Locate every blood parasite and identify its species.
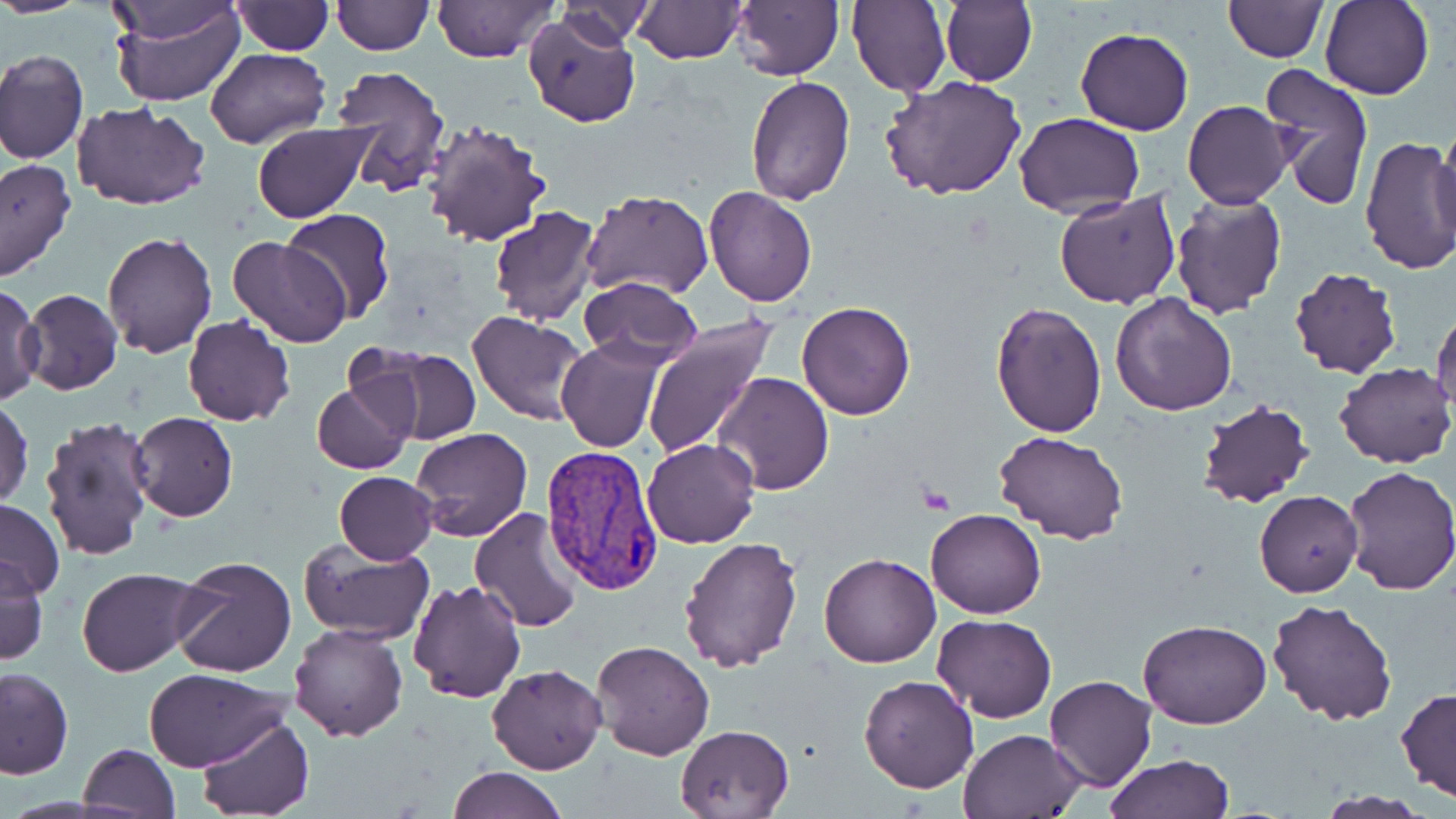

Approximate bounding boxes as named x1/y1/x2/y2 corners in pixels.
Plasmodium vivax-infected red blood cells: (x1=538, y1=447, x2=665, y2=597).
No Plasmodium falciparum, Plasmodium ovale, Plasmodium malariae, Babesia divergens, or Trypanosoma brucei observed.

slide-level diagnosis = Plasmodium vivax
preparation = thin blood smear
modality = light microscopy
field of view = single
stain = May-Grünwald-Giemsa
uninfected red blood cell locations = approximate bounding boxes as named x1/y1/x2/y2 corners in pixels: (x1=0, y1=0, x2=88, y2=18), (x1=108, y1=0, x2=246, y2=109), (x1=330, y1=0, x2=432, y2=55), (x1=732, y1=0, x2=844, y2=81), (x1=849, y1=0, x2=951, y2=98), (x1=940, y1=0, x2=1037, y2=87), (x1=1224, y1=0, x2=1327, y2=61), (x1=1321, y1=0, x2=1435, y2=101), (x1=103, y1=1, x2=247, y2=47), (x1=231, y1=1, x2=333, y2=54), (x1=429, y1=1, x2=558, y2=62), (x1=551, y1=1, x2=655, y2=51), (x1=635, y1=1, x2=744, y2=63), (x1=524, y1=11, x2=640, y2=128), (x1=1075, y1=27, x2=1193, y2=135), (x1=205, y1=48, x2=328, y2=148), (x1=0, y1=50, x2=87, y2=166), (x1=1260, y1=62, x2=1376, y2=210), (x1=329, y1=63, x2=452, y2=197), (x1=880, y1=74, x2=1027, y2=200), (x1=744, y1=75, x2=855, y2=207), (x1=1183, y1=100, x2=1291, y2=206), (x1=72, y1=102, x2=210, y2=211), (x1=1013, y1=111, x2=1145, y2=217), (x1=420, y1=117, x2=551, y2=248), (x1=252, y1=121, x2=373, y2=223), (x1=1434, y1=128, x2=1456, y2=239), (x1=1359, y1=137, x2=1456, y2=275), (x1=0, y1=158, x2=75, y2=283), (x1=702, y1=186, x2=818, y2=307), (x1=582, y1=190, x2=714, y2=300), (x1=1054, y1=192, x2=1182, y2=309), (x1=1170, y1=192, x2=1288, y2=319), (x1=490, y1=207, x2=600, y2=326), (x1=281, y1=210, x2=396, y2=324), (x1=101, y1=231, x2=216, y2=357), (x1=227, y1=237, x2=351, y2=348), (x1=1288, y1=268, x2=1402, y2=381), (x1=578, y1=276, x2=701, y2=368), (x1=1, y1=284, x2=43, y2=404), (x1=20, y1=288, x2=122, y2=395), (x1=1110, y1=292, x2=1238, y2=415), (x1=992, y1=300, x2=1107, y2=436), (x1=796, y1=302, x2=917, y2=421), (x1=1432, y1=306, x2=1456, y2=416), (x1=468, y1=310, x2=591, y2=425), (x1=182, y1=315, x2=296, y2=427), (x1=641, y1=316, x2=776, y2=460), (x1=556, y1=338, x2=667, y2=453), (x1=360, y1=345, x2=481, y2=445), (x1=1334, y1=363, x2=1455, y2=468), (x1=713, y1=372, x2=834, y2=494), (x1=313, y1=382, x2=413, y2=474), (x1=1, y1=396, x2=34, y2=509), (x1=1193, y1=397, x2=1316, y2=510), (x1=128, y1=413, x2=238, y2=522), (x1=39, y1=418, x2=158, y2=564), (x1=410, y1=428, x2=532, y2=543), (x1=994, y1=430, x2=1128, y2=544), (x1=642, y1=438, x2=759, y2=549), (x1=1339, y1=464, x2=1456, y2=595), (x1=334, y1=470, x2=437, y2=564), (x1=1255, y1=490, x2=1362, y2=598), (x1=0, y1=499, x2=65, y2=599), (x1=468, y1=506, x2=586, y2=633), (x1=925, y1=509, x2=1047, y2=618), (x1=678, y1=535, x2=803, y2=674), (x1=299, y1=538, x2=435, y2=642), (x1=819, y1=553, x2=941, y2=668), (x1=0, y1=555, x2=48, y2=664), (x1=169, y1=556, x2=296, y2=678), (x1=77, y1=567, x2=200, y2=677), (x1=408, y1=578, x2=527, y2=703), (x1=1267, y1=600, x2=1398, y2=725), (x1=932, y1=615, x2=1056, y2=722), (x1=1139, y1=618, x2=1272, y2=730), (x1=288, y1=622, x2=408, y2=742), (x1=589, y1=640, x2=715, y2=760), (x1=487, y1=663, x2=607, y2=774), (x1=142, y1=666, x2=290, y2=772), (x1=0, y1=668, x2=73, y2=779), (x1=858, y1=674, x2=980, y2=792), (x1=1044, y1=675, x2=1157, y2=791), (x1=1396, y1=687, x2=1456, y2=802), (x1=195, y1=715, x2=314, y2=819), (x1=675, y1=723, x2=796, y2=817), (x1=962, y1=729, x2=1087, y2=818), (x1=77, y1=743, x2=181, y2=818), (x1=1106, y1=754, x2=1235, y2=818), (x1=446, y1=766, x2=567, y2=819), (x1=1313, y1=791, x2=1437, y2=819)
image size = 1456×819 pixels
platelet locations = approximate bounding boxes as named x1/y1/x2/y2 corners in pixels: (x1=919, y1=485, x2=955, y2=513)
magnification = 1000x